Classify this cell by malaria status.
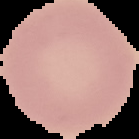
It is uninfected.

Segmented cell region on a black background. From a thin blood film. Image is 139×139 pixels.